Assess the morphology of the red blood cells.
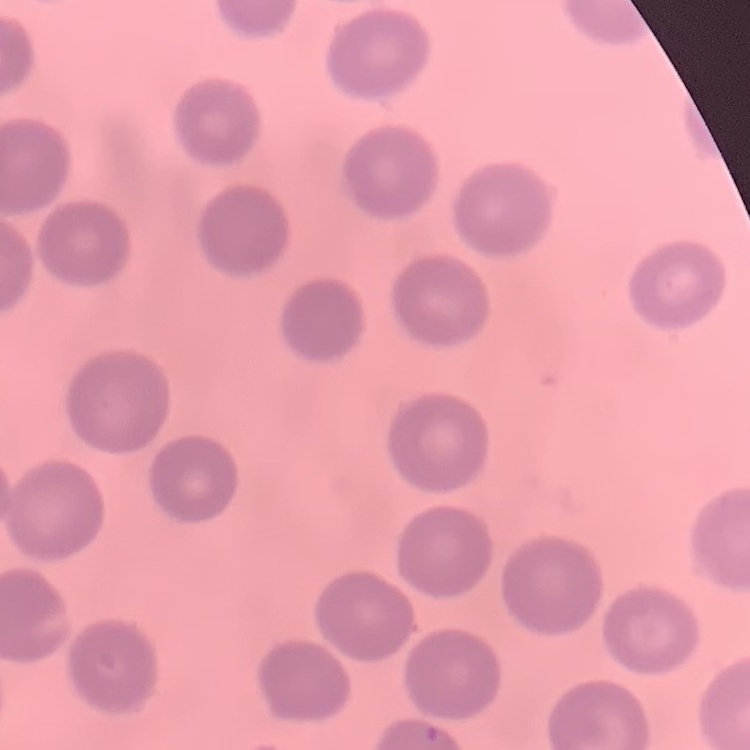

No rouleaux formation.

Square crop of a larger photomicrograph. Stained with either Field's or Giemsa. Thin blood smear.